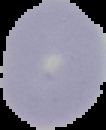
{
  "preparation": "thin blood smear",
  "result": "no malaria parasites seen",
  "image_size": "106×130 pixels",
  "image_type": "segmented cell region on a black background"
}